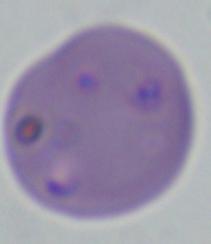
identification = Babesia
modality = micrograph
magnification = 1000x